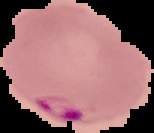

Summary:
  - Result: malaria parasites detected
  - Image size: 154×133 pixels
  - Image type: cell region segmented out of the field of view; surrounding area masked to black
  - Preparation: thin blood film